Assess this cell for malaria.
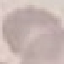
Uninfected.

Summary:
  - Capture: smartphone through the microscope eyepiece
  - Stain: Giemsa
  - Preparation: thin blood film
  - Image type: automatically extracted cell patch, resized to 64 × 64 pixels